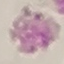

Summary:
  - Malaria status: uninfected
  - Image type: cell patch, automatically extracted from a larger field of view and resized to 64 × 64 pixels
  - Stain: Giemsa
  - Preparation: thin blood film
  - Capture: smartphone through the microscope eyepiece